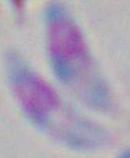
{
  "identification": "Toxoplasma gondii",
  "modality": "micrograph",
  "magnification": "1000x"
}